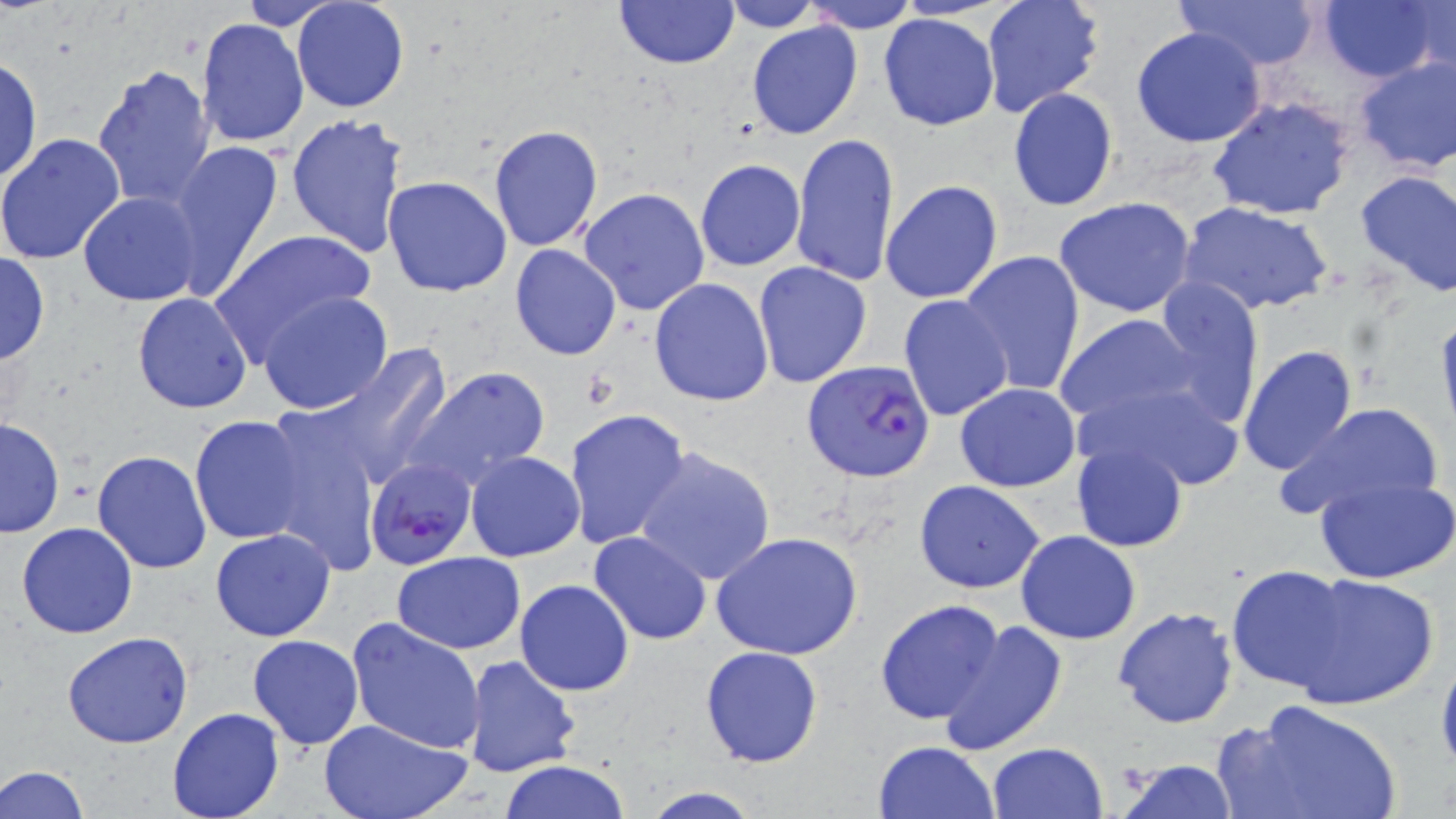

Summary:
  - Coordinate format: approximate bounding boxes as (x1, y1, x2, y2) in pixels
  - Plasmodium falciparum-infected red blood cell locations: (801, 360, 936, 484), (365, 457, 479, 572)
  - Uninfected red blood cell locations: (614, 0, 739, 68), (802, 0, 918, 33), (981, 0, 1106, 118), (1175, 0, 1323, 70), (1319, 0, 1443, 83), (1404, 0, 1454, 79), (233, 1, 346, 30), (290, 1, 411, 113), (718, 1, 823, 31), (878, 13, 998, 131), (196, 18, 309, 148), (745, 19, 863, 141), (1131, 26, 1268, 148), (1351, 56, 1456, 175), (0, 57, 42, 186), (92, 64, 217, 209), (1008, 88, 1118, 211), (1206, 95, 1357, 221), (286, 114, 408, 259), (487, 124, 603, 252), (790, 131, 900, 288), (0, 132, 124, 265), (165, 139, 286, 302), (694, 158, 806, 271), (1355, 168, 1456, 297), (383, 175, 512, 297), (879, 179, 1003, 305), (578, 187, 710, 316), (78, 192, 202, 307), (1054, 198, 1199, 318), (1178, 200, 1337, 316), (210, 228, 375, 360), (510, 243, 623, 360), (958, 250, 1086, 398), (0, 252, 50, 366), (752, 261, 872, 388), (648, 277, 776, 407), (1150, 280, 1268, 429), (256, 292, 393, 415), (132, 293, 253, 412), (898, 295, 1014, 423), (1054, 311, 1209, 429), (1434, 312, 1456, 442), (1238, 344, 1358, 476), (311, 345, 453, 495), (402, 366, 551, 490), (1072, 376, 1244, 492), (954, 383, 1081, 492), (1274, 401, 1445, 525), (565, 408, 691, 551), (260, 414, 381, 574), (189, 415, 308, 544), (0, 417, 64, 538), (1069, 440, 1189, 553), (631, 444, 777, 585), (92, 451, 212, 574), (465, 451, 584, 562), (1315, 473, 1456, 584), (914, 479, 1046, 593), (16, 523, 138, 639), (210, 529, 337, 642), (712, 530, 863, 662), (1015, 530, 1140, 644), (588, 531, 711, 644), (393, 552, 524, 653), (1226, 564, 1353, 694), (1285, 571, 1440, 707), (515, 579, 634, 696), (874, 598, 1006, 724), (1112, 606, 1239, 729), (347, 617, 487, 755), (938, 621, 1066, 754), (63, 632, 194, 750), (247, 635, 363, 750), (699, 644, 824, 768), (1435, 646, 1456, 783), (462, 654, 582, 778), (1220, 697, 1404, 819), (167, 706, 285, 819), (319, 716, 472, 819), (875, 740, 999, 819), (988, 742, 1108, 819), (1116, 758, 1237, 818), (500, 759, 630, 819), (1, 765, 89, 819), (640, 787, 764, 819)
  - Slide-level diagnosis: Plasmodium falciparum
  - Image size: 1456×819 pixels
  - Field of view: one of a larger specimen
  - Modality: light microscopy
  - Stain: May-Grünwald-Giemsa
  - Preparation: thin blood smear
  - Magnification: 1000x